Report the malaria status of this cell.
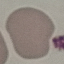
Uninfected.

Summary:
  - Preparation: thin smear
  - Image type: automatically extracted cell patch, resized to 64 × 64 pixels
  - Stain: Giemsa
  - Capture: smartphone camera at the microscope eyepiece